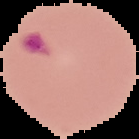

Summary:
  - Image type: segmented cell region with the area outside set to black
  - Preparation: thin blood film
  - Image size: 139×139 pixels
  - Result: Plasmodium parasites detected